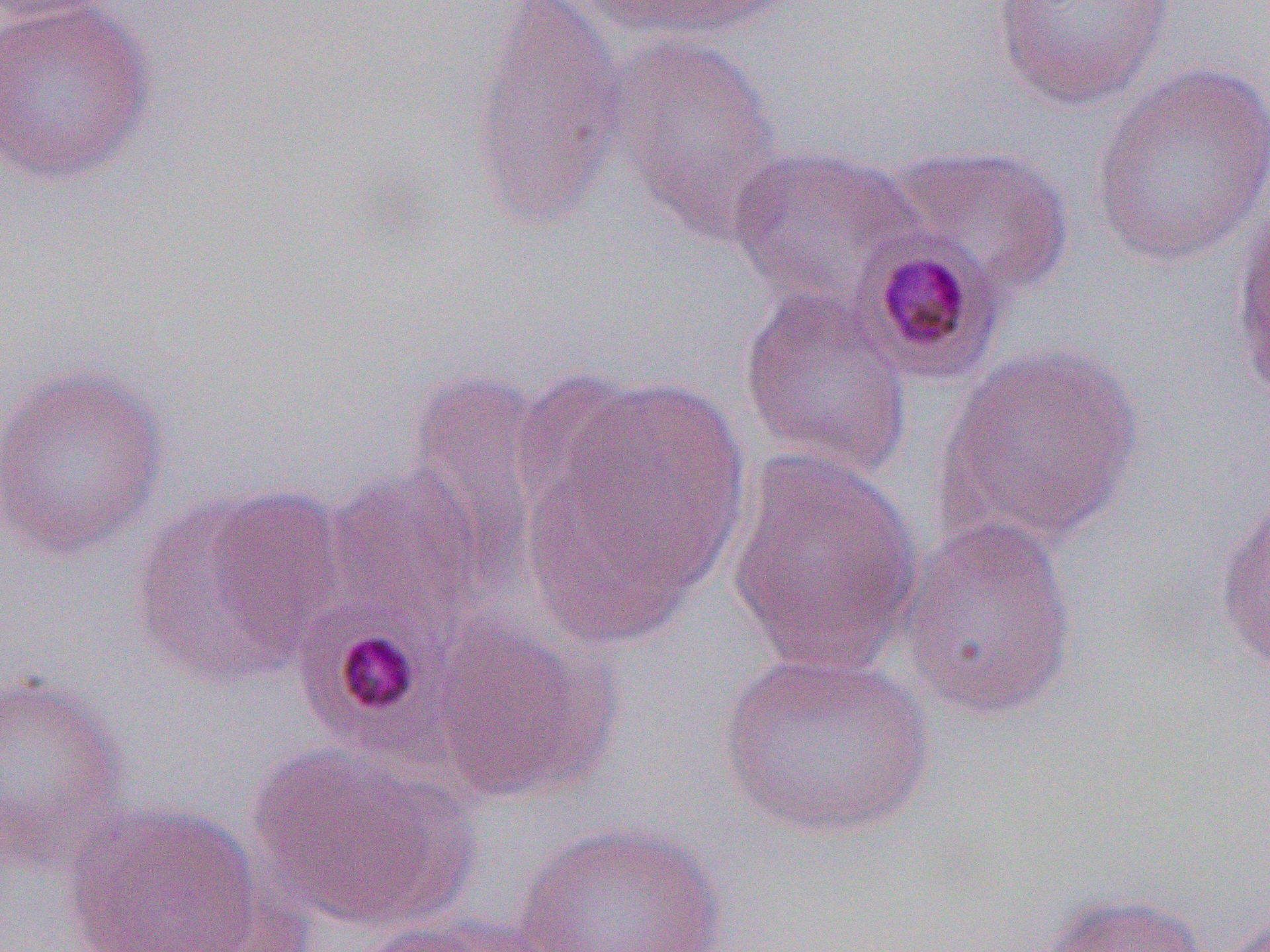
Summary:
  - Coordinate format: approximate bounding boxes as [x1, y1, x2, y2] in pixels
  - Platelet locations: [293, 605, 440, 753]
  - Uninfected red blood cell locations: [0, 0, 127, 26], [0, 0, 158, 186], [466, 0, 627, 233], [573, 0, 792, 44], [989, 0, 1179, 111], [603, 31, 783, 237], [1089, 61, 1270, 269], [885, 143, 1075, 299], [725, 144, 926, 310], [1229, 193, 1270, 417], [737, 285, 914, 482], [935, 342, 1146, 552], [0, 363, 168, 561], [405, 365, 553, 580], [526, 375, 749, 638], [722, 447, 923, 674], [323, 463, 492, 635], [129, 483, 344, 690], [1213, 490, 1270, 677], [895, 512, 1081, 721], [428, 615, 619, 804], [717, 649, 937, 840], [0, 672, 131, 875], [247, 743, 477, 933], [62, 800, 268, 952], [510, 821, 727, 952], [1036, 893, 1211, 952], [1220, 907, 1270, 952], [353, 913, 561, 951]
  - Plasmodium malariae-infected red blood cell locations: [852, 233, 1010, 387]
  - Slide-level diagnosis: Plasmodium malariae
  - Field of view: single
  - Modality: optical microscopy
  - Magnification: 1000x
  - Image size: 1270×952 pixels
  - Preparation: thin blood smear